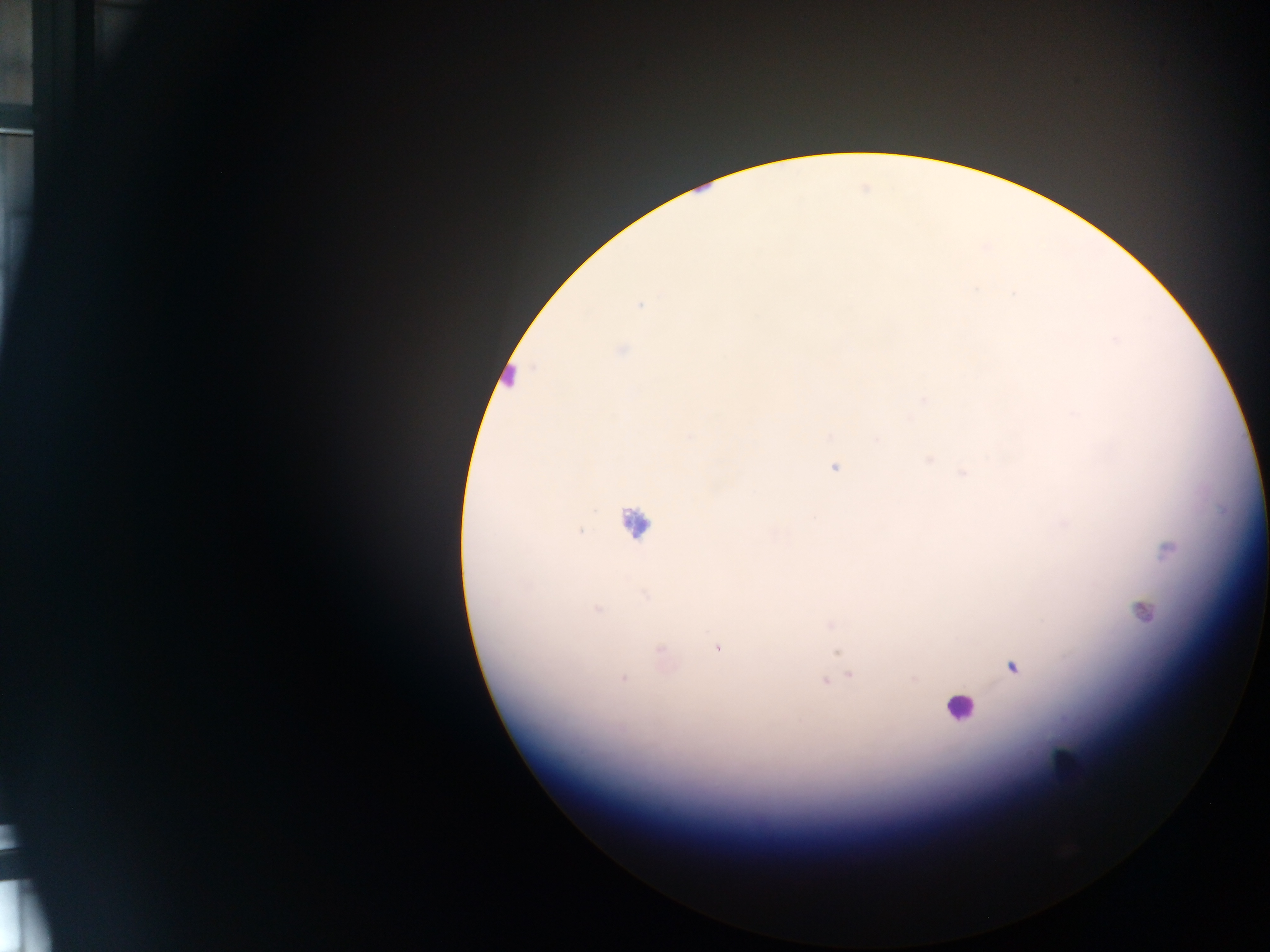
field of view = single
preparation = thick blood smear
image size = 1270×952 pixels
Plasmodium parasite locations = approximate centers as x y in pixels: 1134 6; 640 306; 620 350; 924 399; 878 440; 929 458; 835 466; 963 472; 1168 550; 596 608; 1142 611; 831 623; 718 647; 838 652; 661 654; 1013 667; 850 675; 623 677; 912 677; 825 680
leukocyte locations = approximate centers as x y in pixels: 509 378; 634 524; 960 708; 1067 764
capture = mobile-phone photograph through a microscope
country = Ghana